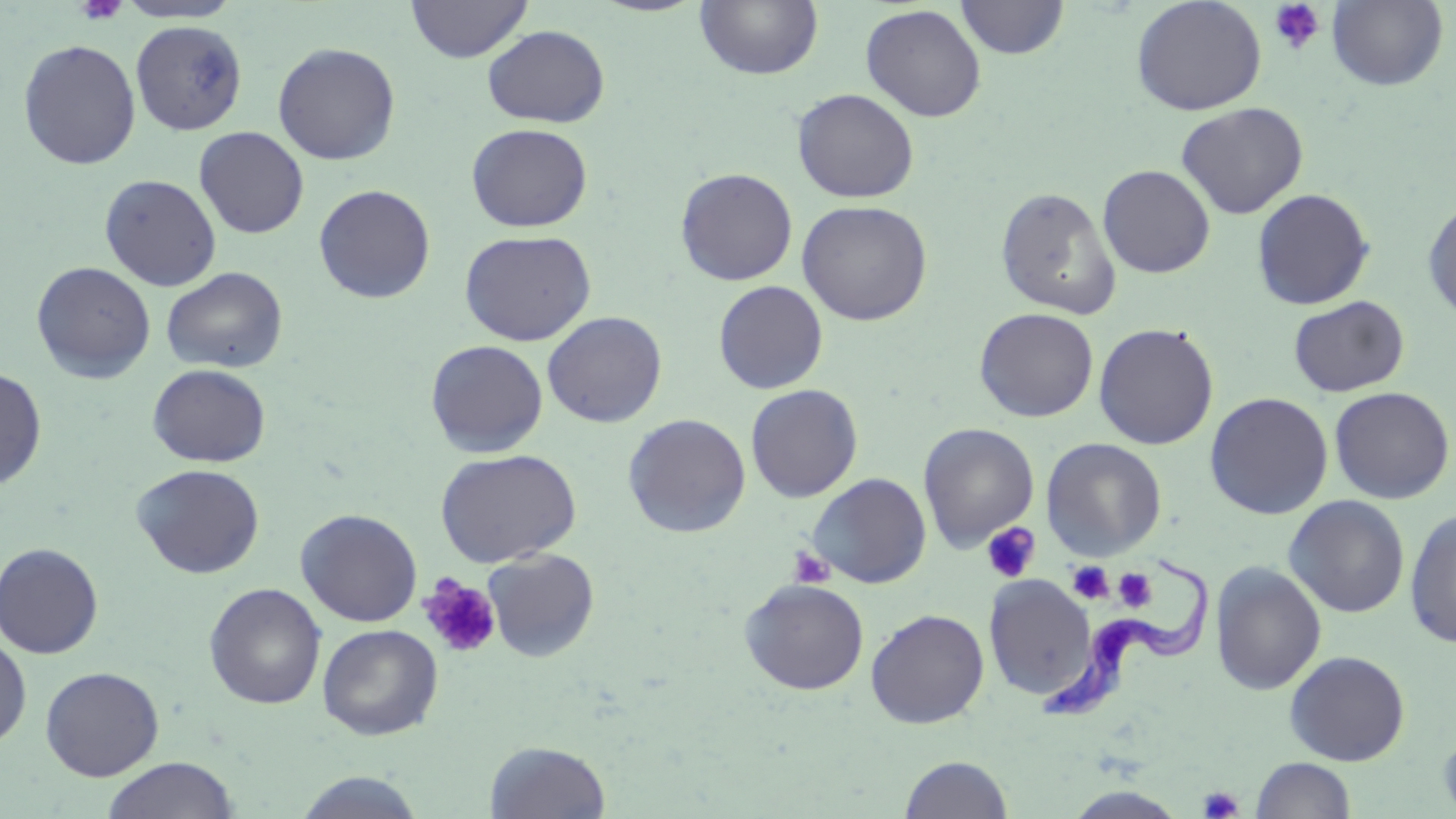

Summary:
  - Coordinate format: approximate bounding boxes as named x1/y1/x2/y2 corners in pixels
  - Trypanosoma brucei locations: (x1=1038, y1=547, x2=1211, y2=720)
  - Uninfected red blood cell locations: (x1=115, y1=0, x2=243, y2=24), (x1=405, y1=0, x2=533, y2=62), (x1=695, y1=0, x2=823, y2=80), (x1=955, y1=0, x2=1070, y2=59), (x1=1131, y1=0, x2=1267, y2=116), (x1=1327, y1=0, x2=1449, y2=90), (x1=860, y1=4, x2=987, y2=123), (x1=130, y1=20, x2=248, y2=136), (x1=482, y1=25, x2=610, y2=128), (x1=17, y1=39, x2=141, y2=170), (x1=272, y1=41, x2=401, y2=165), (x1=792, y1=88, x2=919, y2=203), (x1=1175, y1=102, x2=1308, y2=219), (x1=466, y1=123, x2=592, y2=232), (x1=194, y1=126, x2=309, y2=239), (x1=1098, y1=164, x2=1215, y2=278), (x1=675, y1=167, x2=797, y2=286), (x1=99, y1=173, x2=221, y2=291), (x1=313, y1=184, x2=436, y2=304), (x1=995, y1=186, x2=1121, y2=320), (x1=1251, y1=188, x2=1375, y2=310), (x1=1422, y1=196, x2=1456, y2=325), (x1=796, y1=199, x2=933, y2=326), (x1=459, y1=229, x2=596, y2=346), (x1=31, y1=261, x2=156, y2=383), (x1=161, y1=266, x2=288, y2=373), (x1=713, y1=280, x2=828, y2=395), (x1=1288, y1=295, x2=1410, y2=397), (x1=974, y1=307, x2=1098, y2=422), (x1=542, y1=311, x2=667, y2=428), (x1=1093, y1=322, x2=1219, y2=450), (x1=425, y1=340, x2=548, y2=458), (x1=148, y1=363, x2=271, y2=467), (x1=0, y1=368, x2=47, y2=491), (x1=745, y1=383, x2=863, y2=503), (x1=1329, y1=386, x2=1454, y2=504), (x1=1204, y1=392, x2=1333, y2=520), (x1=623, y1=413, x2=751, y2=537), (x1=918, y1=423, x2=1039, y2=552), (x1=1041, y1=438, x2=1167, y2=561), (x1=434, y1=449, x2=581, y2=568), (x1=132, y1=463, x2=266, y2=579), (x1=807, y1=473, x2=932, y2=588), (x1=1284, y1=496, x2=1409, y2=618), (x1=1404, y1=506, x2=1456, y2=648), (x1=296, y1=508, x2=422, y2=626), (x1=0, y1=542, x2=104, y2=659), (x1=482, y1=549, x2=600, y2=662), (x1=1210, y1=561, x2=1327, y2=695), (x1=985, y1=575, x2=1096, y2=700), (x1=738, y1=578, x2=870, y2=696), (x1=204, y1=583, x2=326, y2=709), (x1=865, y1=608, x2=989, y2=728), (x1=317, y1=624, x2=443, y2=741), (x1=0, y1=633, x2=32, y2=749), (x1=1284, y1=650, x2=1410, y2=766), (x1=40, y1=666, x2=164, y2=780), (x1=1438, y1=723, x2=1456, y2=819), (x1=485, y1=740, x2=612, y2=818), (x1=899, y1=754, x2=1014, y2=818), (x1=101, y1=757, x2=238, y2=819), (x1=1251, y1=757, x2=1356, y2=818), (x1=292, y1=770, x2=428, y2=818)
  - Platelet locations: (x1=74, y1=0, x2=128, y2=25), (x1=1268, y1=0, x2=1326, y2=54), (x1=981, y1=522, x2=1040, y2=583), (x1=789, y1=547, x2=834, y2=588), (x1=1067, y1=560, x2=1114, y2=605), (x1=1113, y1=568, x2=1157, y2=612), (x1=418, y1=575, x2=502, y2=660), (x1=1198, y1=786, x2=1244, y2=818)
  - Slide-level diagnosis: Trypanosoma brucei
  - Image size: 1456×819 pixels
  - Modality: light microscopy
  - Preparation: thin blood smear
  - Stain: May-Grünwald-Giemsa
  - Field of view: one of a larger specimen
  - Magnification: 1000x